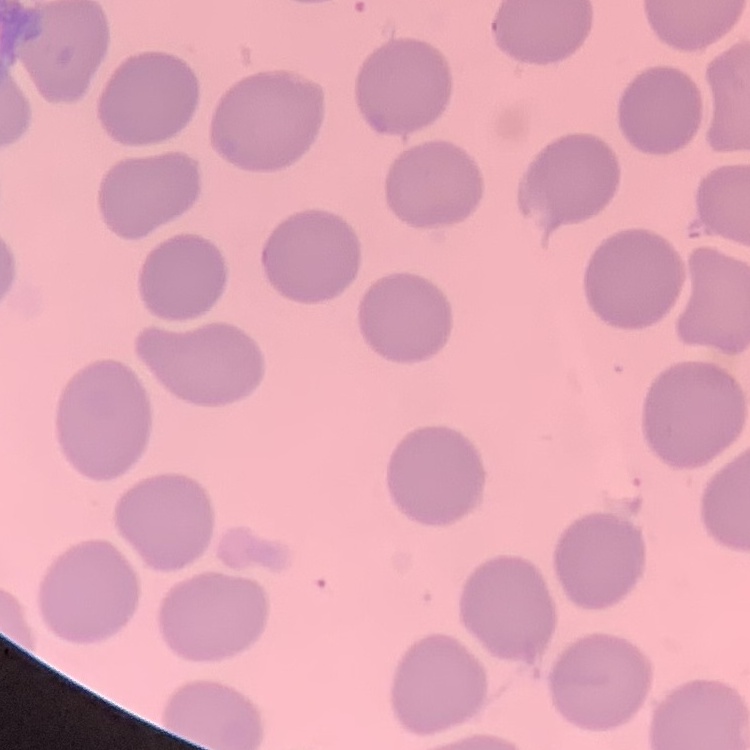

red blood cell morphology = no rouleaux formation
preparation = thin blood smear
image type = square crop of a larger photomicrograph
stain = Field's or Giemsa